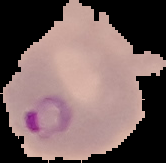
image type = cell region segmented out of the field of view; surrounding area masked to black
preparation = thin blood smear
image size = 166×163 pixels
malaria status = parasitized